Identify the cell.
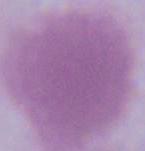
This is an erythrocyte.

modality = photomicrograph
magnification = 1000x